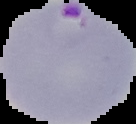

Summary:
  - Image size: 136×124 pixels
  - Image type: segmented cell region with the area outside set to black
  - Result: malaria parasites detected
  - Preparation: thin blood smear